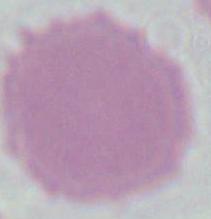
Summary:
  - Modality: micrograph
  - Magnification: 1000x
  - Identification: red blood cell